Report the malaria status of this cell.
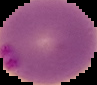
It is parasitized.

From a thin blood film. Image is 97×85 pixels. Segmented cell region on a black background.